Give the position of every Plasmodium falciparum parasite, noting its life-cycle stage.
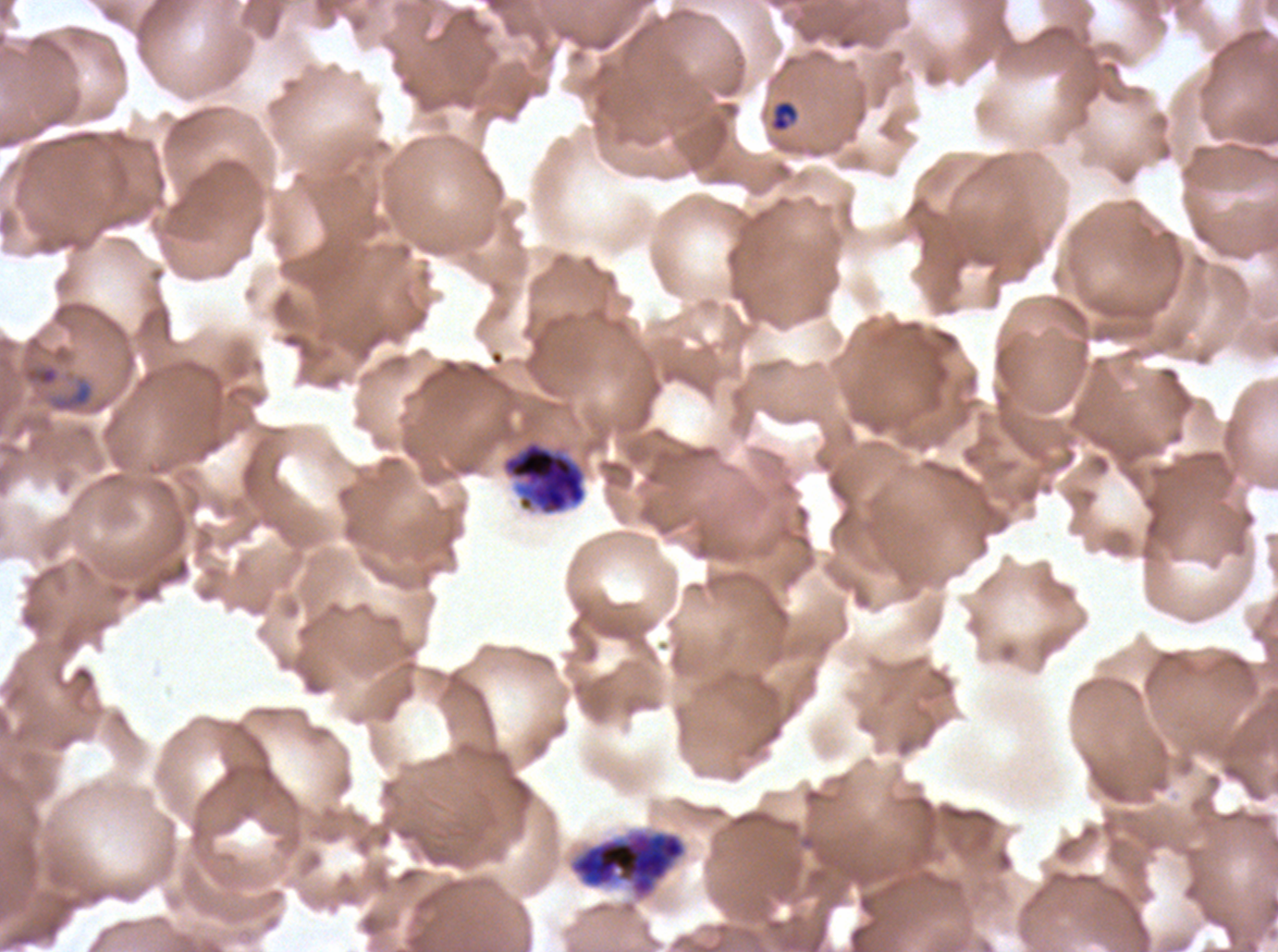
Approximate bounding rectangles given as corner coordinates in pixels from the top-left.
Rings: (x1=25, y1=365, x2=59, y2=386).
Late-ring/early-trophozoite forms: (x1=771, y1=101, x2=797, y2=131).
Early schizonts: (x1=500, y1=439, x2=587, y2=516), (x1=568, y1=827, x2=687, y2=901).
No mid trophozoites, late trophozoites, late schizonts, segmenters, or gametocytes observed.

Summary:
  - Field of view: one sub-image of a larger composite
  - Image size: 1278×952 pixels
  - Specimen: ex-vivo Plasmodium falciparum culture from a patient in The Gambia, grown for 24 to 48 hours
  - Life-cycle stages observed: ring, late-ring/early-trophozoite, early schizont
  - Stain: Giemsa
  - Preparation: thin blood film